Report the malaria status of this cell.
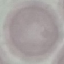
Uninfected.

Giemsa-stained preparation. Acquired by smartphone through the microscope eyepiece. Automatically extracted cell patch, resized to 64 × 64 pixels. Thin smear of blood.